Give the extent of all uninfected red blood cells.
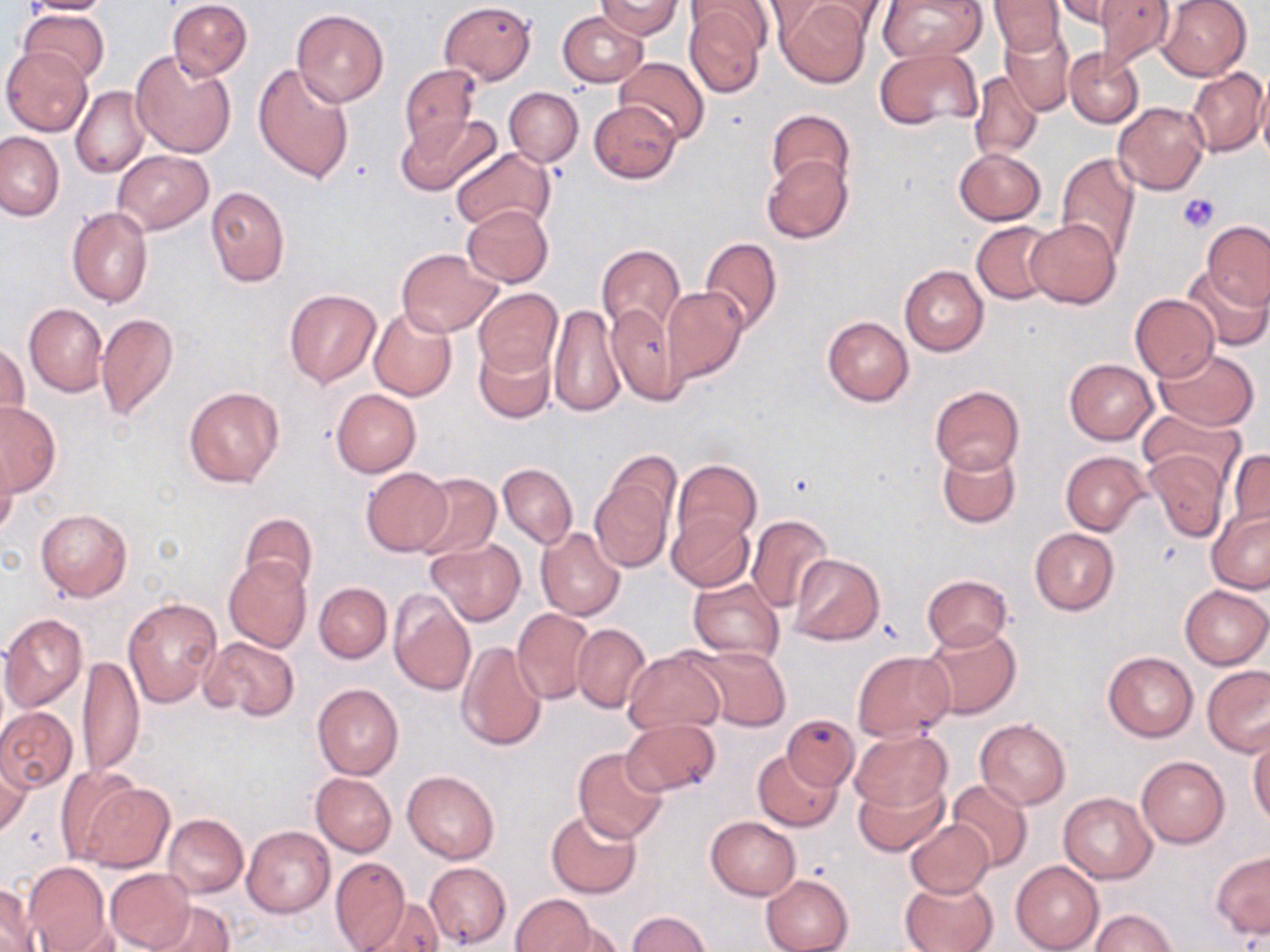
Approximate bounding boxes as [x1, y1, x2, y2] in pixels.
Uninfected red blood cells: [20, 0, 116, 15], [167, 0, 253, 79], [776, 0, 872, 89], [806, 0, 896, 39], [877, 0, 985, 66], [1095, 0, 1174, 70], [1158, 0, 1251, 80], [595, 1, 682, 39], [755, 1, 837, 43], [990, 1, 1064, 56], [439, 2, 536, 84], [1054, 2, 1130, 28], [682, 3, 768, 98], [18, 9, 109, 83], [291, 9, 389, 106], [558, 11, 647, 87], [999, 23, 1076, 116], [1, 47, 92, 137], [130, 48, 238, 158], [873, 48, 982, 129], [1064, 49, 1144, 127], [615, 56, 710, 144], [253, 63, 355, 184], [398, 63, 482, 147], [1187, 67, 1267, 157], [967, 70, 1042, 162], [1257, 78, 1270, 166], [71, 86, 148, 179], [505, 87, 583, 166], [590, 100, 682, 182], [1114, 102, 1209, 195], [766, 109, 854, 194], [398, 113, 503, 196], [0, 132, 63, 220], [449, 148, 554, 232], [954, 148, 1046, 225], [114, 151, 212, 233], [760, 153, 852, 243], [1056, 153, 1140, 262], [205, 185, 290, 287], [462, 205, 553, 287], [67, 207, 153, 307], [1025, 218, 1122, 308], [1201, 220, 1270, 307], [971, 221, 1059, 305], [699, 236, 783, 335], [597, 244, 686, 334], [397, 248, 504, 338], [899, 265, 989, 356], [1182, 266, 1269, 351], [473, 287, 563, 378], [663, 287, 747, 383], [283, 289, 382, 387], [1130, 294, 1220, 381], [607, 300, 683, 405], [24, 304, 107, 395], [548, 306, 623, 416], [369, 307, 457, 401], [96, 314, 178, 423], [822, 316, 914, 406], [473, 340, 554, 422], [0, 341, 28, 430], [1155, 348, 1260, 431], [1064, 359, 1157, 444], [930, 384, 1025, 475], [182, 387, 284, 488], [331, 390, 420, 476], [0, 401, 61, 496], [1140, 408, 1244, 490], [938, 446, 1021, 529], [1143, 448, 1229, 543], [1226, 448, 1270, 535], [0, 449, 17, 535], [1060, 451, 1149, 535], [672, 461, 760, 549], [497, 463, 577, 549], [361, 468, 453, 556], [590, 472, 675, 572], [412, 473, 500, 563], [36, 508, 131, 601], [1206, 509, 1269, 593], [667, 511, 754, 591], [239, 513, 318, 594], [745, 515, 834, 613], [534, 528, 626, 622], [1029, 528, 1120, 614], [426, 539, 525, 627], [788, 554, 884, 644], [224, 557, 311, 652], [921, 575, 1011, 651], [688, 577, 784, 662], [315, 583, 391, 662], [1180, 585, 1269, 669], [388, 589, 475, 696], [124, 597, 221, 707], [512, 607, 594, 704], [1, 614, 88, 713], [571, 624, 650, 711], [920, 624, 1021, 720], [202, 636, 299, 722], [456, 640, 547, 753], [689, 645, 790, 731], [624, 648, 726, 735], [852, 651, 956, 741], [1102, 651, 1198, 741], [76, 656, 145, 778], [1202, 665, 1270, 755], [312, 684, 403, 781], [0, 707, 77, 792], [784, 715, 855, 789], [620, 718, 721, 797], [975, 718, 1070, 809], [850, 727, 951, 815], [1248, 733, 1269, 825], [572, 747, 669, 843], [1, 749, 32, 836], [754, 750, 843, 831], [1135, 754, 1230, 848], [56, 766, 146, 863], [402, 770, 499, 863], [311, 772, 395, 856], [854, 778, 947, 856], [947, 780, 1033, 871], [80, 782, 173, 873], [1058, 792, 1156, 883], [546, 810, 641, 897], [163, 814, 249, 898], [705, 816, 800, 901], [905, 819, 995, 898], [243, 826, 334, 917], [1211, 850, 1269, 941], [329, 856, 410, 952], [23, 861, 113, 952], [1011, 861, 1104, 952], [424, 862, 511, 947], [104, 869, 194, 948], [760, 874, 853, 952], [899, 878, 998, 952], [1, 883, 39, 950], [511, 894, 597, 952], [359, 897, 442, 951], [144, 899, 234, 952], [1090, 909, 1178, 952], [627, 910, 712, 951], [547, 927, 626, 952].

Summary:
  - Platelet locations: [1179, 193, 1218, 233]
  - Slide-level diagnosis: negative for blood parasites
  - Magnification: 1000x
  - Stain: May-Grünwald-Giemsa
  - Preparation: thin blood film
  - Field of view: one of a larger specimen
  - Image size: 1270×952 pixels
  - Modality: optical microscopy